Locate and identify every blood parasite.
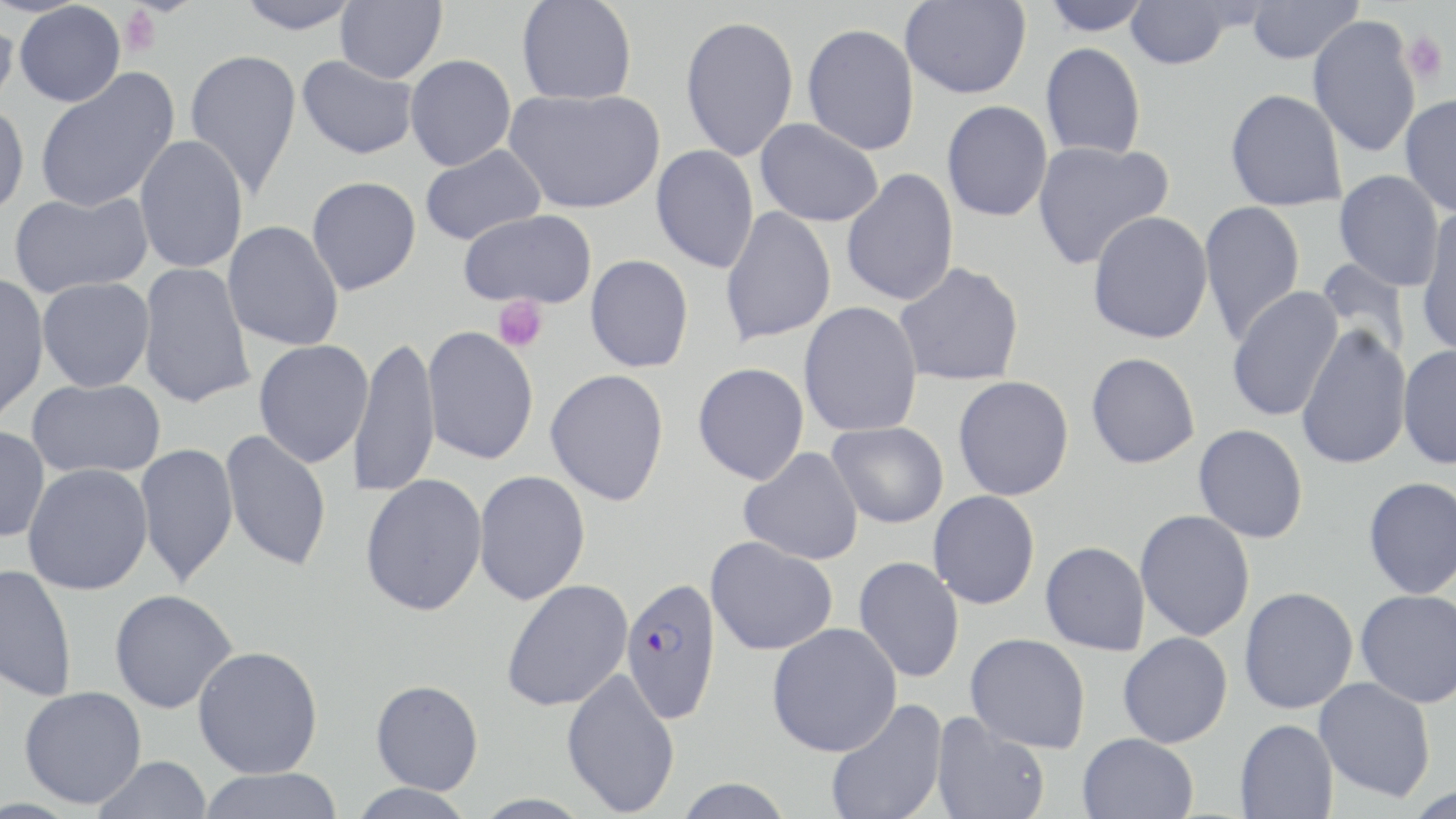

Approximate bounding boxes as (x1, y1, x2, y2) in pixels.
Plasmodium falciparum-infected red blood cells: (620, 577, 723, 723).
No Plasmodium ovale, Plasmodium malariae, Plasmodium vivax, Babesia divergens, or Trypanosoma brucei observed.

Summary:
  - Platelet locations: (118, 5, 164, 57), (1401, 31, 1449, 83), (492, 296, 548, 353)
  - Uninfected red blood cell locations: (232, 0, 363, 34), (335, 0, 446, 83), (517, 0, 637, 105), (900, 0, 1031, 99), (1039, 0, 1154, 35), (1246, 0, 1362, 64), (1125, 1, 1233, 69), (14, 2, 126, 107), (0, 10, 20, 118), (679, 14, 799, 162), (1308, 15, 1421, 158), (802, 23, 920, 155), (1040, 42, 1146, 160), (184, 48, 302, 199), (405, 54, 516, 171), (297, 55, 418, 159), (35, 68, 180, 214), (505, 87, 665, 214), (1225, 89, 1348, 211), (1400, 94, 1456, 216), (941, 100, 1053, 222), (0, 101, 29, 218), (755, 118, 883, 227), (134, 135, 248, 274), (1032, 140, 1174, 270), (420, 144, 546, 246), (651, 145, 759, 273), (841, 168, 959, 307), (1334, 170, 1445, 291), (306, 176, 422, 296), (9, 190, 153, 297), (1199, 200, 1305, 345), (720, 207, 836, 347), (458, 209, 597, 309), (1415, 210, 1456, 356), (1087, 211, 1213, 344), (223, 221, 344, 351), (585, 254, 694, 373), (1317, 258, 1411, 361), (137, 262, 256, 409), (894, 263, 1025, 387), (0, 273, 50, 423), (37, 277, 155, 392), (1226, 286, 1345, 422), (799, 301, 923, 437), (1296, 324, 1412, 470), (422, 326, 539, 465), (348, 335, 441, 498), (254, 340, 373, 467), (1398, 343, 1456, 469), (1086, 352, 1200, 469), (692, 362, 809, 485), (545, 369, 670, 506), (953, 375, 1074, 501), (27, 378, 167, 478), (827, 421, 949, 528), (1193, 424, 1309, 543), (0, 426, 51, 542), (220, 429, 333, 572), (134, 442, 239, 588), (739, 447, 864, 566), (23, 463, 153, 595), (473, 470, 591, 605), (360, 474, 488, 616), (1363, 477, 1456, 599), (928, 490, 1041, 610), (1135, 509, 1255, 642), (705, 537, 838, 656), (1040, 541, 1150, 655), (853, 555, 965, 684), (0, 564, 77, 702), (501, 579, 633, 712), (1238, 586, 1359, 714), (109, 589, 238, 713), (1356, 589, 1456, 708), (767, 622, 902, 756), (1117, 631, 1233, 748), (965, 633, 1091, 753), (193, 645, 324, 778), (561, 668, 681, 817), (1314, 677, 1436, 802), (370, 679, 483, 795), (18, 686, 147, 809), (825, 698, 948, 819), (930, 713, 1050, 819), (1234, 718, 1338, 818), (1077, 732, 1199, 819), (92, 755, 213, 819), (196, 768, 345, 819), (671, 778, 795, 819), (347, 783, 477, 818)
  - Slide-level diagnosis: Plasmodium falciparum
  - Magnification: 1000x
  - Stain: May-Grünwald-Giemsa
  - Field of view: one of a larger specimen
  - Modality: optical microscopy
  - Image size: 1456×819 pixels
  - Preparation: thin blood smear